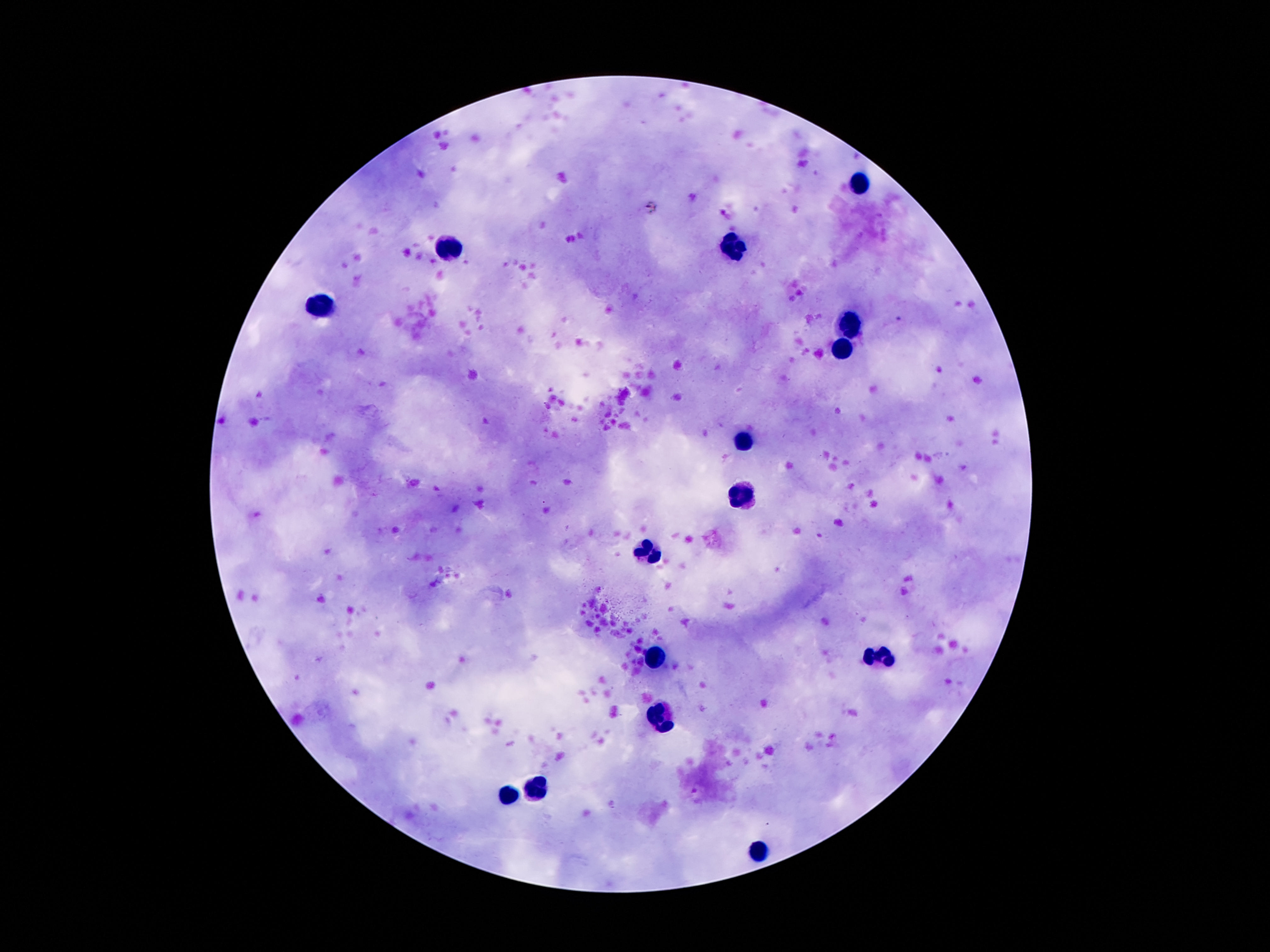

{
  "field_of_view": "single",
  "capture": "smartphone camera through the microscope eyepiece",
  "patient_malaria_status": "negative",
  "stain": "Giemsa",
  "preparation": "thick blood film",
  "magnification": "100x",
  "image_size": "1270×952 pixels",
  "leukocyte_locations": "approximate object centers, in pixels from the top-left corner: (x=857, y=182), (x=448, y=248), (x=737, y=248), (x=316, y=307), (x=846, y=323), (x=841, y=350), (x=741, y=446), (x=739, y=496), (x=650, y=549), (x=882, y=656), (x=655, y=657), (x=664, y=716), (x=539, y=786), (x=507, y=797), (x=757, y=851)"
}